Outline each blood parasite and name the species.
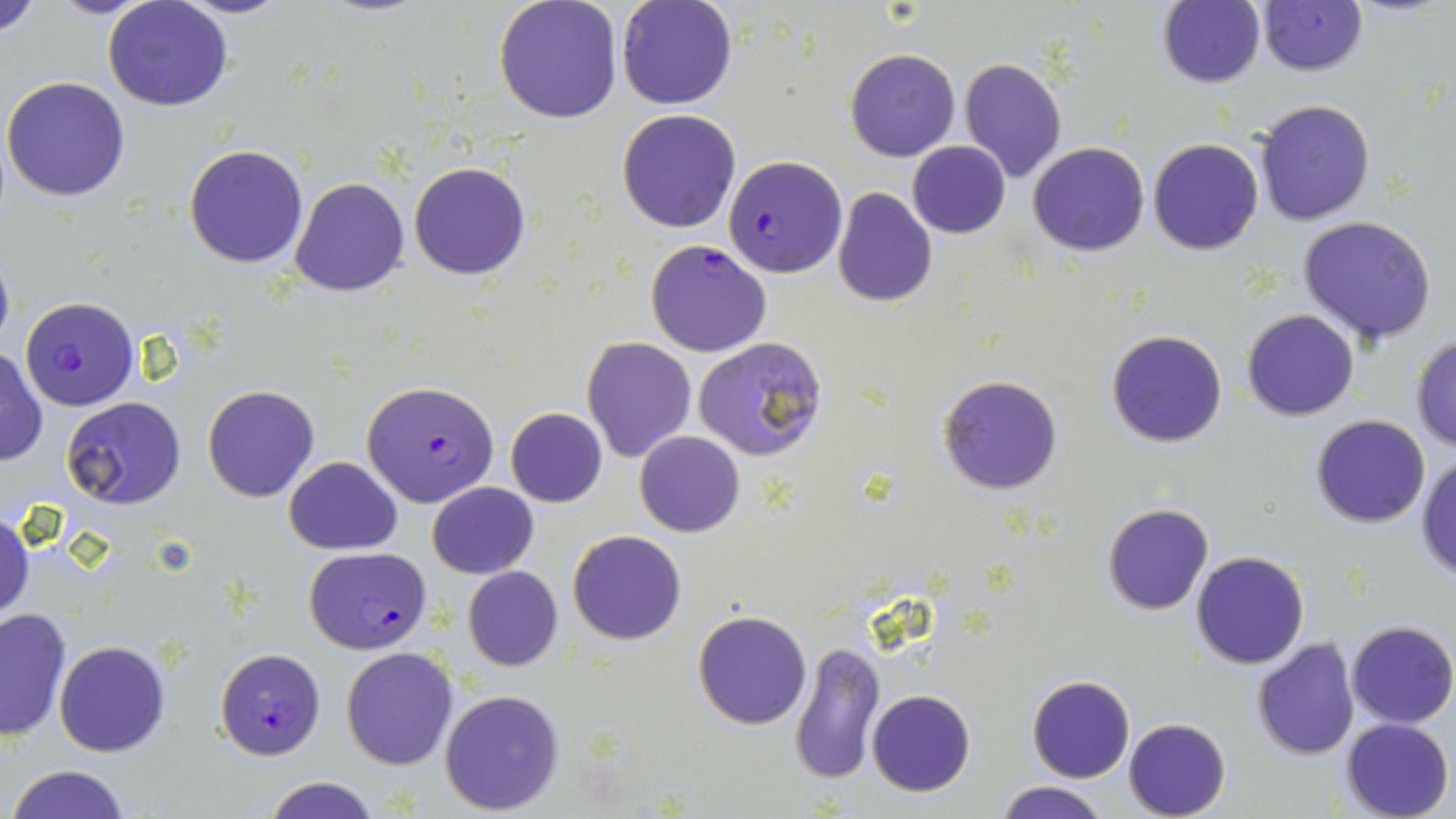
Approximate bounding boxes as (x1,y1)-(x2,y2) corner pairs in pixels.
Plasmodium falciparum-infected red blood cells: (722,155)-(847,277), (644,240)-(771,357), (19,296)-(139,411), (362,380)-(498,506), (302,546)-(431,654), (215,647)-(326,759).
No Plasmodium ovale, Plasmodium malariae, Plasmodium vivax, Babesia divergens, or Trypanosoma brucei observed.

Uninfected red blood cell locations: (0,0)-(47,41), (49,0)-(159,19), (102,0)-(234,111), (174,0)-(293,18), (616,0)-(740,110), (1159,0)-(1266,88), (1257,0)-(1367,75), (493,1)-(622,123), (846,48)-(961,161), (959,58)-(1067,184), (2,76)-(131,202), (1255,97)-(1375,226), (617,110)-(741,232), (1149,137)-(1263,255), (907,141)-(1011,238), (1029,141)-(1147,256), (185,144)-(309,267), (409,162)-(529,281), (289,175)-(410,296), (831,188)-(937,308), (1298,214)-(1438,345), (0,246)-(14,357), (1242,308)-(1359,421), (1105,329)-(1228,447), (1409,334)-(1456,452), (583,336)-(697,462), (693,336)-(830,463), (0,346)-(47,467), (937,374)-(1063,495), (203,384)-(319,502), (64,396)-(185,510), (506,407)-(608,507), (1309,414)-(1432,528), (635,431)-(745,538), (1416,454)-(1456,582), (283,456)-(401,554), (429,481)-(537,578), (1103,503)-(1215,615), (0,510)-(35,622), (568,531)-(687,644), (1190,550)-(1309,668), (463,566)-(563,671), (1,606)-(72,742), (693,610)-(812,729), (1346,621)-(1455,729), (1251,637)-(1361,760), (790,639)-(885,786), (54,640)-(171,757), (341,646)-(458,769), (1025,674)-(1135,783), (440,689)-(565,812), (867,689)-(976,796), (1123,717)-(1232,819), (1340,718)-(1454,819), (8,765)-(132,819), (262,775)-(383,819), (992,781)-(1112,819). Slide-level diagnosis: Plasmodium falciparum. Captured at 1000x magnification. Image is 1456×819 pixels. May-Grünwald-Giemsa-stained preparation. Thin blood smear. Single field of view. Light microscopy.